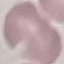

Summary:
  - Malaria status: uninfected
  - Image type: cell patch, automatically extracted from a larger field of view and resized to 64 × 64 pixels
  - Preparation: thin smear
  - Capture: smartphone through the microscope eyepiece
  - Stain: Giemsa